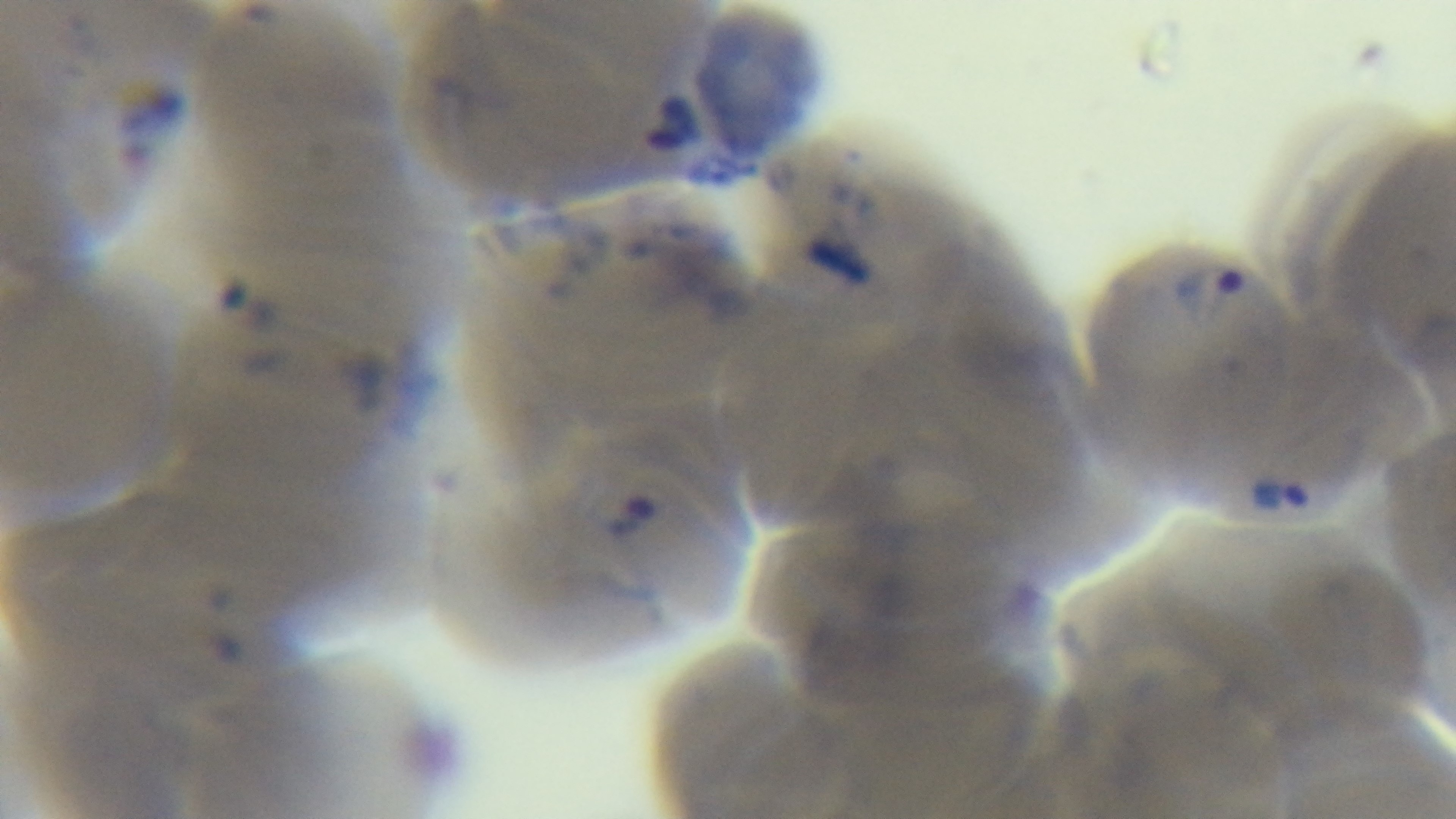 Malaria status: positive. Preparation: thin blood film. Single field of view. Giemsa stain. Oil-immersion objective, 100x. Captured with a mounted 4K digital camera. Light microscopy.